Classify this cell by malaria status.
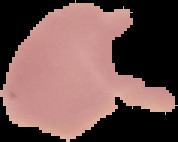

It is uninfected.

preparation = thin blood smear
image type = segmented cell region on a black background
image size = 178×142 pixels